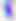

Summary:
  - Magnification: 400x
  - Modality: micrograph
  - Identification: Toxoplasma gondii